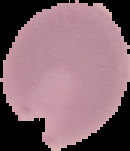

Summary:
  - Preparation: thin blood smear
  - Image size: 130×151 pixels
  - Image type: segmented cell region with the area outside set to black
  - Malaria status: parasitized